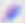

Summary:
  - Modality: micrograph
  - Identification: Toxoplasma gondii
  - Magnification: 400x